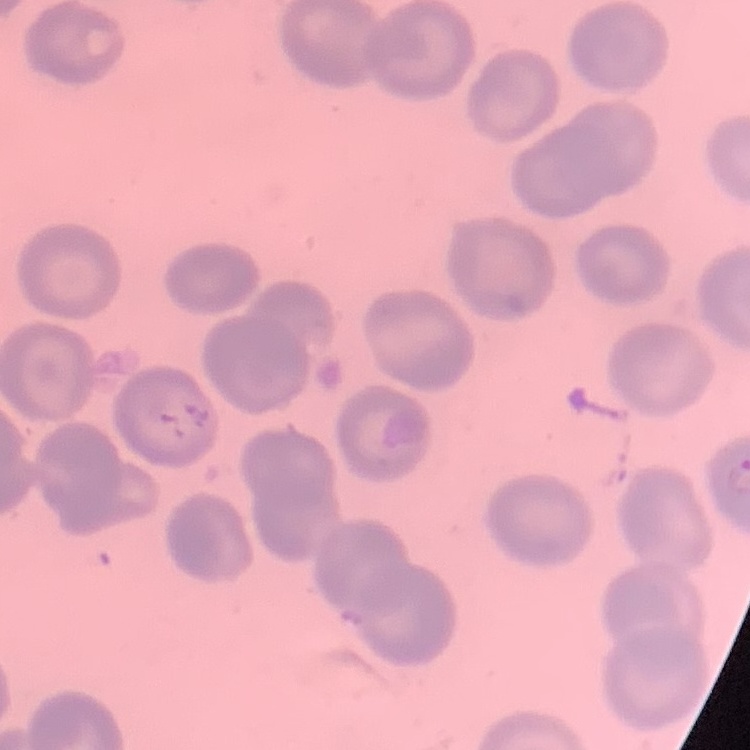 The erythrocytes show no rouleaux formation. Thin peripheral smear. Stained with either Field's or Giemsa. Square crop of a larger photomicrograph.